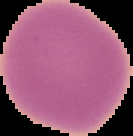

{
  "image_type": "segmented cell region with the area outside set to black",
  "preparation": "thin blood smear",
  "image_size": "133×136 pixels",
  "malaria_status": "uninfected"
}